Locate every parasitized RBC.
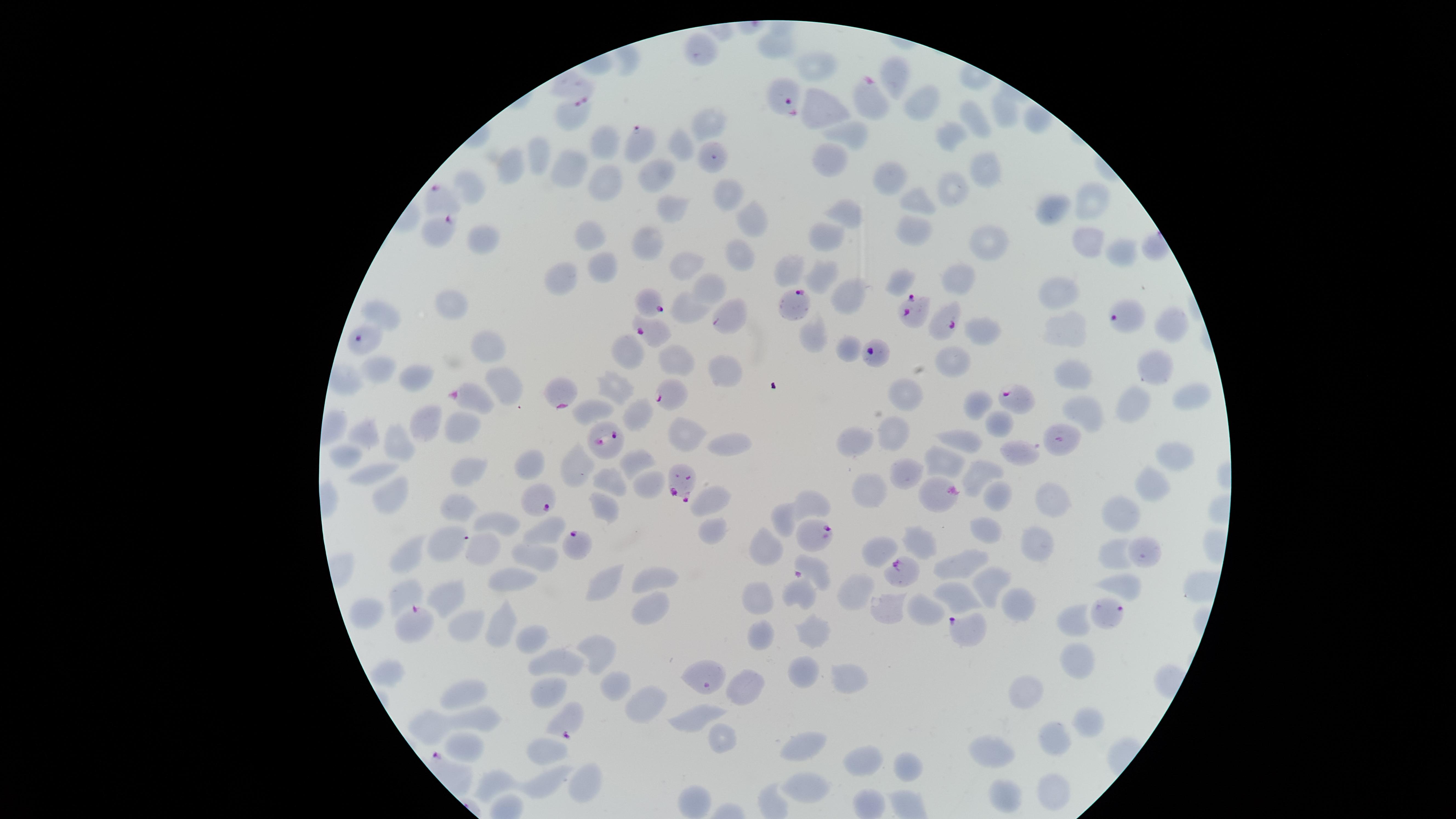
Approximate marker points as {x, y} in pixels.
Parasitized RBCs: {868, 99}, {788, 101}, {574, 113}, {638, 143}, {449, 201}, {436, 229}, {646, 298}, {793, 305}, {911, 308}, {728, 316}, {1127, 317}, {943, 322}, {648, 331}, {365, 334}, {877, 354}, {563, 390}, {668, 395}, {470, 397}, {1015, 399}, {608, 437}, {1058, 439}, {684, 480}, {542, 495}, {817, 533}, {572, 542}, {900, 571}, {1107, 609}, {418, 615}, {961, 626}.

Approximate marker points as {x, y} in pixels. Uninfected RBCs: {821, 67}, {893, 76}, {918, 105}, {817, 106}, {1003, 111}, {706, 119}, {977, 121}, {843, 132}, {948, 133}, {676, 135}, {604, 144}, {827, 152}, {539, 157}, {512, 168}, {983, 171}, {568, 173}, {662, 179}, {886, 181}, {469, 182}, {601, 189}, {948, 191}, {724, 194}, {916, 202}, {1090, 202}, {844, 207}, {665, 210}, {1048, 211}, {754, 216}, {904, 232}, {828, 234}, {646, 235}, {481, 236}, {589, 236}, {1086, 241}, {983, 244}, {1122, 252}, {736, 255}, {601, 265}, {786, 267}, {685, 269}, {818, 270}, {565, 272}, {959, 277}, {894, 280}, {707, 287}, {1057, 293}, {842, 294}, {450, 302}, {693, 305}, {383, 313}, {1165, 320}, {1063, 331}, {815, 335}, {976, 336}, {483, 347}, {846, 350}, {627, 351}, {676, 361}, {953, 362}, {1152, 363}, {1070, 369}, {381, 370}, {718, 373}, {416, 377}, {507, 380}, {614, 388}, {908, 393}, {1187, 401}, {982, 404}, {1129, 406}, {1083, 408}, {592, 411}, {636, 413}, {996, 420}, {425, 423}, {458, 429}, {368, 431}, {683, 431}, {891, 432}, {964, 437}, {394, 441}, {736, 441}, {851, 442}, {1019, 449}, {343, 455}, {1168, 455}, {937, 462}, {577, 463}, {632, 463}, {531, 467}, {368, 471}, {465, 473}, {608, 480}, {901, 480}, {642, 486}, {1151, 486}, {869, 489}, {385, 493}, {931, 493}, {713, 495}, {1001, 495}, {812, 502}, {1060, 503}, {602, 504}, {457, 508}, {1118, 514}, {786, 516}, {501, 520}, {547, 524}, {984, 532}, {709, 533}, {1041, 540}, {917, 542}, {441, 544}, {769, 545}, {472, 549}, {876, 549}, {414, 552}, {1110, 554}, {537, 555}, {1138, 556}, {963, 563}, {654, 578}, {512, 580}, {1121, 586}, {854, 587}, {598, 588}, {984, 588}, {404, 592}, {442, 595}, {797, 597}, {758, 601}, {953, 601}, {1010, 607}, {646, 608}, {886, 609}, {919, 610}, {368, 615}, {502, 618}, {1077, 622}, {462, 623}, {812, 629}, {762, 632}, {529, 639}, {601, 650}, {1074, 662}, {564, 664}, {804, 670}, {389, 674}, {844, 674}, {611, 681}, {747, 684}, {541, 689}, {466, 692}, {1025, 698}, {644, 705}, {698, 717}, {479, 721}, {432, 723}, {1088, 724}, {717, 733}, {1053, 738}, {465, 747}, {798, 748}, {546, 752}, {1000, 753}, {860, 759}, {906, 764}, {492, 782}, {588, 782}, {549, 785}, {814, 786}, {1049, 790}, {1007, 798}, {696, 799}. Smartphone photograph through the microscope eyepiece. Thin blood film. Giemsa-stained preparation. Image is 1456×819 pixels. Species: Plasmodium falciparum. The visible region is circular. Single field of view.